Outline each Plasmodium ovale-infected red blood cell.
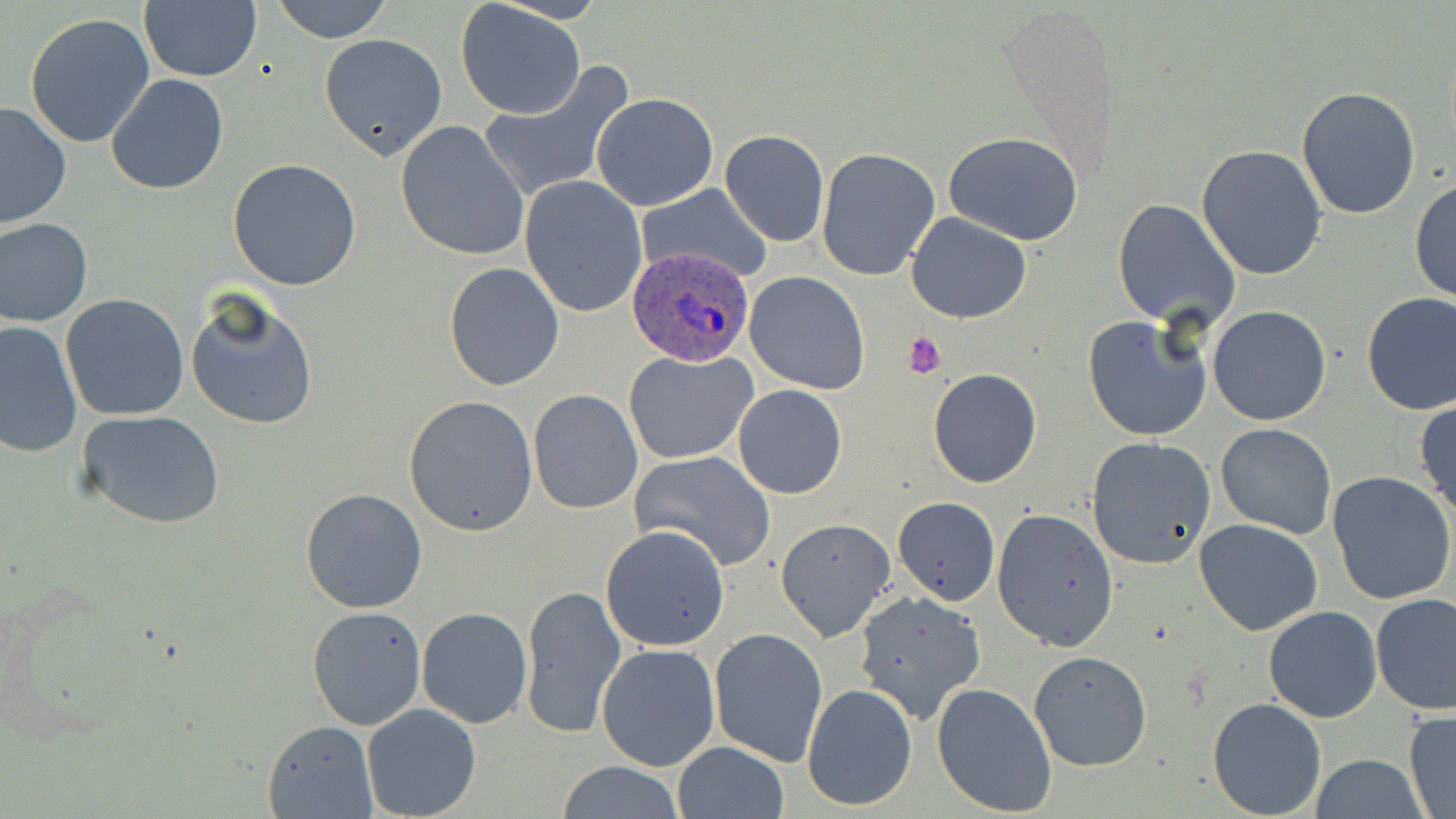

Approximate bounding boxes as [x1, y1, x2, y2] in pixels.
Plasmodium ovale-infected red blood cells: [626, 242, 760, 368].

Uninfected red blood cell locations: [269, 0, 396, 44], [456, 2, 585, 117], [138, 3, 262, 82], [25, 12, 155, 148], [320, 33, 447, 160], [475, 64, 636, 204], [106, 73, 229, 196], [1295, 85, 1422, 219], [591, 92, 718, 210], [0, 101, 72, 232], [394, 119, 531, 263], [718, 129, 830, 246], [942, 131, 1084, 243], [1196, 145, 1328, 281], [816, 148, 940, 280], [227, 157, 362, 291], [519, 175, 649, 318], [1411, 179, 1455, 305], [636, 182, 774, 283], [1112, 198, 1241, 330], [905, 212, 1031, 323], [0, 217, 94, 327], [443, 261, 566, 392], [744, 271, 871, 394], [185, 289, 319, 432], [1361, 292, 1456, 416], [61, 293, 189, 421], [1207, 306, 1331, 428], [1082, 314, 1213, 441], [1, 320, 82, 458], [623, 348, 756, 464], [928, 368, 1042, 487], [732, 385, 847, 499], [527, 388, 642, 514], [403, 395, 539, 537], [1413, 399, 1456, 519], [77, 409, 226, 529], [1214, 422, 1337, 539], [1085, 436, 1216, 569], [629, 450, 777, 573], [1327, 472, 1456, 607], [298, 487, 428, 614], [892, 497, 1000, 605], [991, 508, 1119, 654], [775, 517, 898, 643], [1194, 519, 1323, 635], [600, 524, 730, 650], [519, 583, 626, 737], [852, 589, 985, 722], [1371, 593, 1456, 713], [1263, 605, 1382, 722], [307, 606, 426, 730], [417, 606, 532, 728], [708, 627, 828, 766], [596, 643, 722, 772], [1027, 649, 1152, 772], [931, 682, 1059, 817], [801, 683, 919, 812], [1207, 697, 1328, 818], [361, 704, 483, 819], [1403, 708, 1456, 817], [263, 720, 377, 817], [671, 741, 790, 819], [1308, 753, 1425, 819], [555, 761, 686, 818]. Platelet locations: [901, 331, 947, 378]. Slide-level diagnosis: Plasmodium ovale. Thin blood smear. Image is 1456×819 pixels. Captured at 1000x magnification. Single field of view. May-Grünwald-Giemsa stain. Light microscopy.